Describe the morphology of the red blood cells.
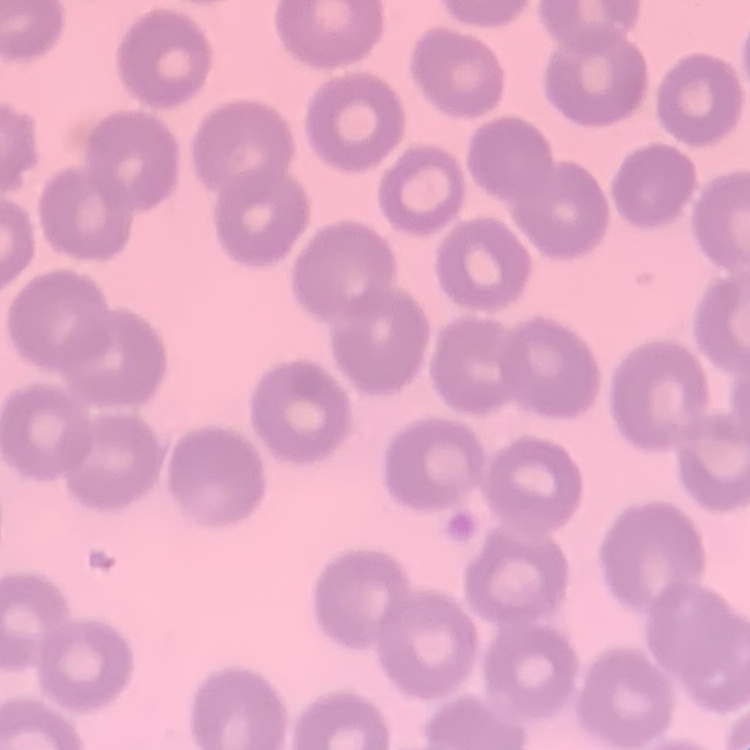

No rouleaux formation.

Square crop of a larger photomicrograph. Stained with either Field's or Giemsa. Thin blood smear.